Assess this cell for malaria.
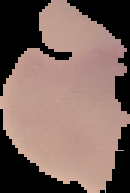

Uninfected.

The area outside the segmented cell region is set to black. Image is 130×193 pixels. From a thin blood film.